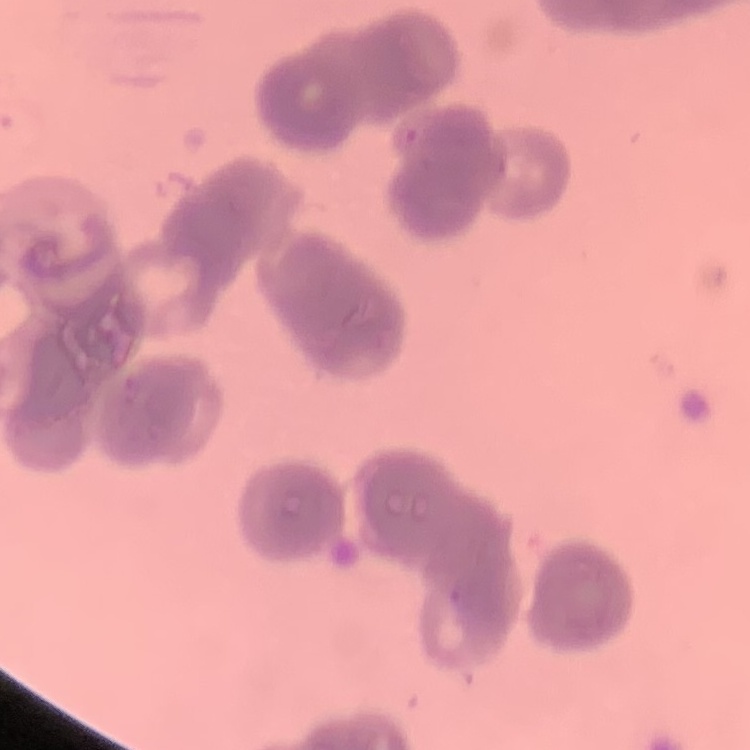
red blood cell morphology = rouleaux formation
image type = one tile cut from a larger photomicrograph
preparation = thin blood smear
stain = Field's or Giemsa